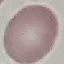
{
  "malaria_status": "uninfected",
  "preparation": "thin blood smear",
  "capture": "smartphone through the microscope eyepiece",
  "image_type": "automatically extracted cell patch, resized to 64 × 64 pixels",
  "stain": "Giemsa"
}